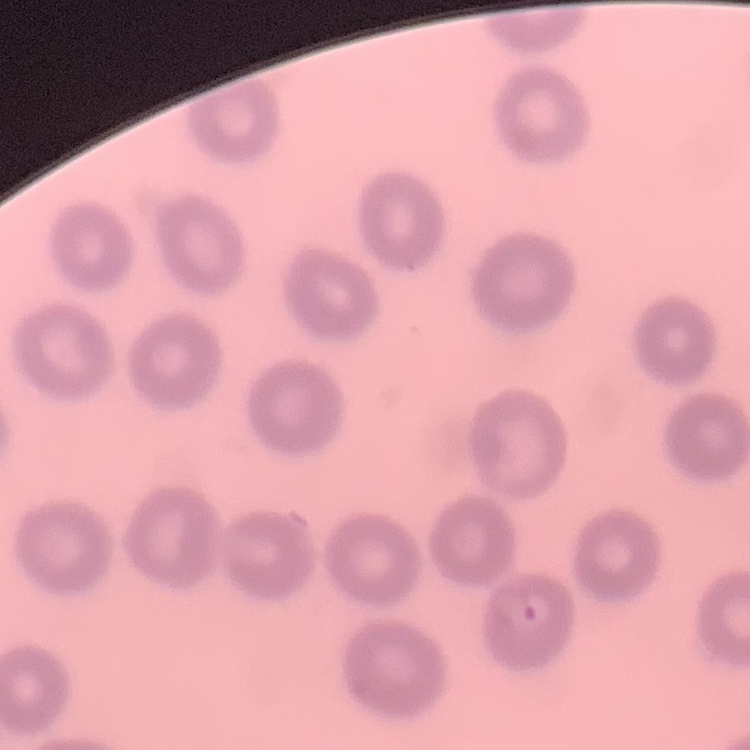

The red blood cells exhibit no rouleaux formation. Thin blood smear. Square crop of a larger photomicrograph. Field's or Giemsa stain.